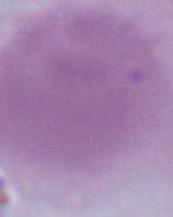
magnification = 1000x
identification = erythrocyte
modality = photomicrograph